Locate and identify every blood parasite.
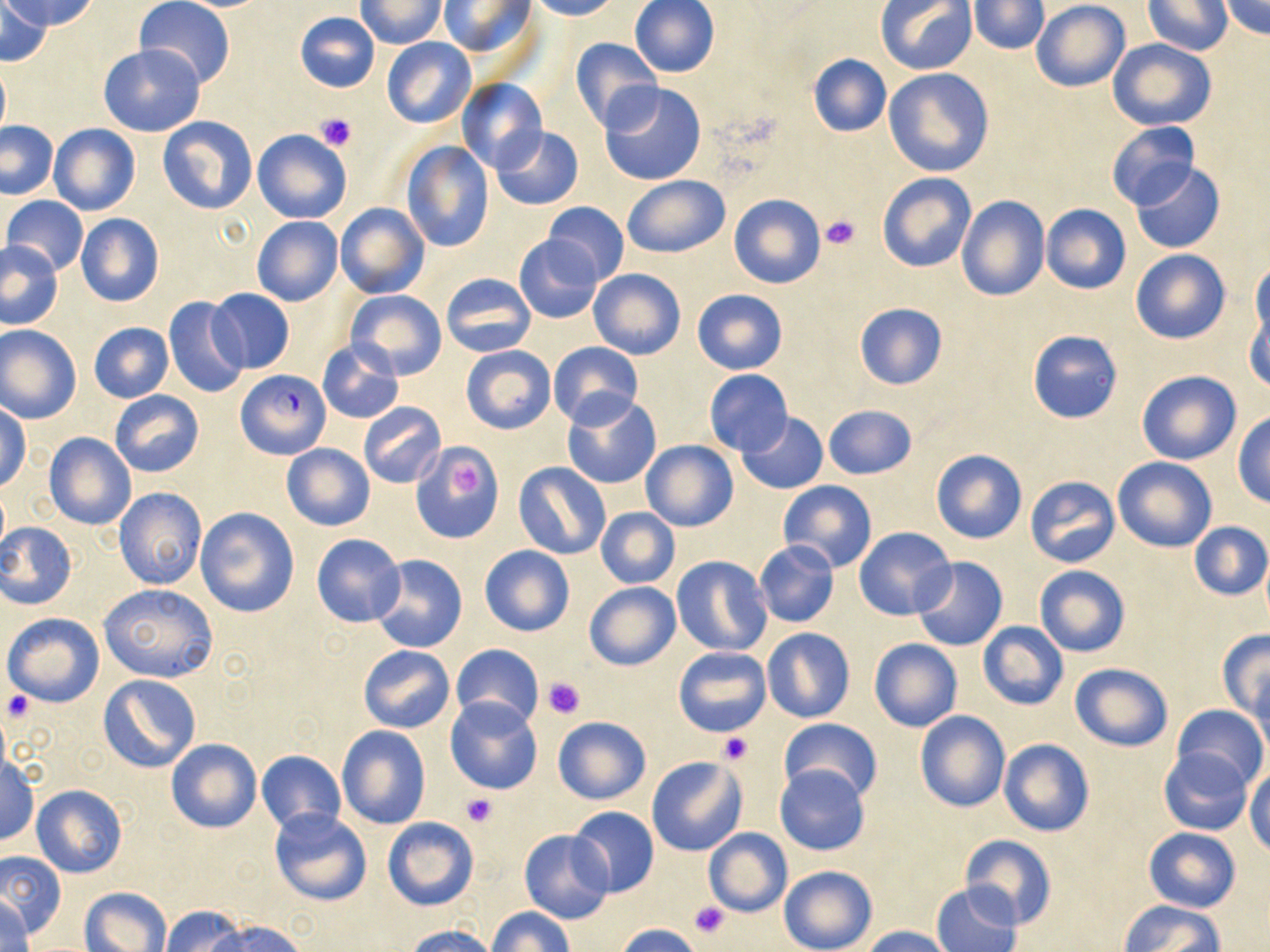
Approximate bounding boxes as [x1, y1, x2, y2] in pixels.
Plasmodium falciparum-infected red blood cells: [237, 369, 331, 459].
No Plasmodium ovale, Plasmodium malariae, Plasmodium vivax, Babesia divergens, or Trypanosoma brucei observed.

Platelet locations: [314, 112, 356, 151], [819, 214, 861, 251], [451, 463, 487, 502], [544, 677, 585, 717], [2, 690, 34, 722], [718, 732, 752, 764], [460, 792, 497, 829], [691, 899, 730, 939]. Uninfected red blood cell locations: [4, 0, 99, 31], [136, 0, 235, 89], [529, 0, 617, 20], [629, 0, 720, 78], [877, 0, 976, 74], [1218, 0, 1270, 39], [1, 1, 53, 65], [356, 1, 445, 48], [438, 1, 537, 61], [969, 1, 1049, 54], [1030, 1, 1130, 91], [1142, 1, 1232, 55], [293, 11, 379, 92], [381, 36, 477, 129], [568, 38, 664, 133], [1108, 38, 1216, 131], [98, 44, 205, 137], [806, 53, 892, 136], [0, 61, 10, 140], [884, 68, 994, 177], [455, 78, 546, 172], [598, 82, 706, 185], [157, 116, 258, 216], [0, 121, 58, 199], [1106, 122, 1199, 211], [48, 123, 140, 217], [491, 126, 583, 211], [252, 129, 351, 224], [400, 142, 495, 251], [1130, 162, 1226, 254], [877, 173, 977, 274], [622, 176, 731, 259], [728, 193, 826, 289], [2, 195, 89, 275], [957, 195, 1050, 301], [542, 201, 628, 285], [335, 202, 430, 299], [1041, 204, 1131, 294], [75, 214, 165, 307], [251, 216, 343, 306], [514, 234, 605, 324], [0, 239, 64, 329], [1131, 249, 1229, 345], [1249, 260, 1269, 348], [588, 268, 686, 360], [440, 273, 537, 357], [207, 288, 295, 374], [346, 289, 446, 380], [691, 289, 788, 374], [164, 296, 249, 398], [854, 302, 947, 390], [1245, 302, 1270, 391], [88, 322, 173, 403], [0, 325, 82, 424], [1028, 331, 1122, 423], [317, 339, 404, 423], [548, 341, 643, 428], [460, 345, 556, 436], [1137, 369, 1242, 465], [704, 370, 793, 455], [110, 390, 204, 478], [562, 394, 661, 489], [358, 401, 446, 488], [0, 403, 30, 493], [822, 404, 917, 479], [736, 412, 828, 495], [1233, 413, 1270, 507], [43, 432, 137, 530], [641, 441, 738, 532], [411, 442, 503, 543], [282, 444, 375, 531], [929, 449, 1026, 544], [1113, 456, 1216, 551], [514, 463, 611, 560], [1025, 475, 1119, 568], [778, 480, 877, 573], [113, 487, 207, 589], [194, 507, 299, 617], [595, 507, 680, 589], [1188, 521, 1269, 601], [0, 522, 77, 609], [854, 526, 956, 621], [312, 532, 406, 627], [754, 541, 839, 627], [479, 545, 574, 637], [370, 555, 468, 654], [671, 556, 772, 658], [911, 556, 1009, 651], [1035, 564, 1130, 657], [583, 582, 680, 671], [98, 583, 218, 682], [2, 612, 105, 707], [977, 621, 1069, 709], [761, 627, 856, 723], [1216, 630, 1270, 720], [869, 639, 963, 732], [450, 643, 542, 729], [358, 645, 454, 733], [673, 647, 771, 737], [1069, 663, 1173, 752], [1250, 670, 1269, 756], [98, 674, 201, 773], [445, 697, 543, 796], [1174, 704, 1267, 787], [914, 710, 1011, 813], [552, 715, 652, 804], [778, 718, 881, 802], [337, 725, 431, 829], [165, 738, 261, 834], [998, 739, 1094, 837], [1158, 746, 1253, 836], [256, 750, 346, 833], [1, 754, 40, 845], [646, 755, 747, 856], [774, 764, 870, 857], [1246, 764, 1270, 856], [31, 785, 127, 878], [568, 805, 659, 897], [268, 807, 372, 906], [383, 817, 479, 911], [518, 828, 615, 924], [703, 828, 792, 916], [1144, 828, 1240, 911], [959, 834, 1057, 930], [0, 848, 66, 939], [778, 864, 877, 952], [931, 882, 1022, 952], [79, 886, 175, 952], [0, 894, 36, 952], [1119, 901, 1222, 951], [159, 906, 247, 952], [488, 907, 572, 952], [209, 920, 305, 952], [614, 923, 707, 952], [401, 924, 503, 952], [861, 926, 960, 952]. Slide-level diagnosis: Plasmodium falciparum. May-Grünwald-Giemsa stain. 1000x magnification. Thin blood film. Image is 1270×952 pixels. Light microscopy. One field of a larger specimen.